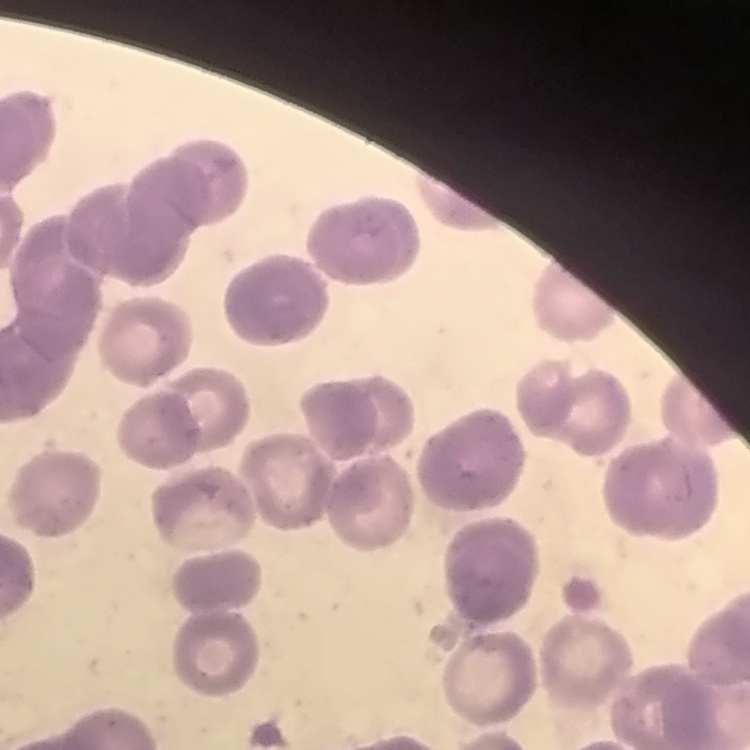
red blood cell morphology = rouleaux formation
image type = square crop of a larger photomicrograph
stain = Field's or Giemsa
preparation = thin blood smear